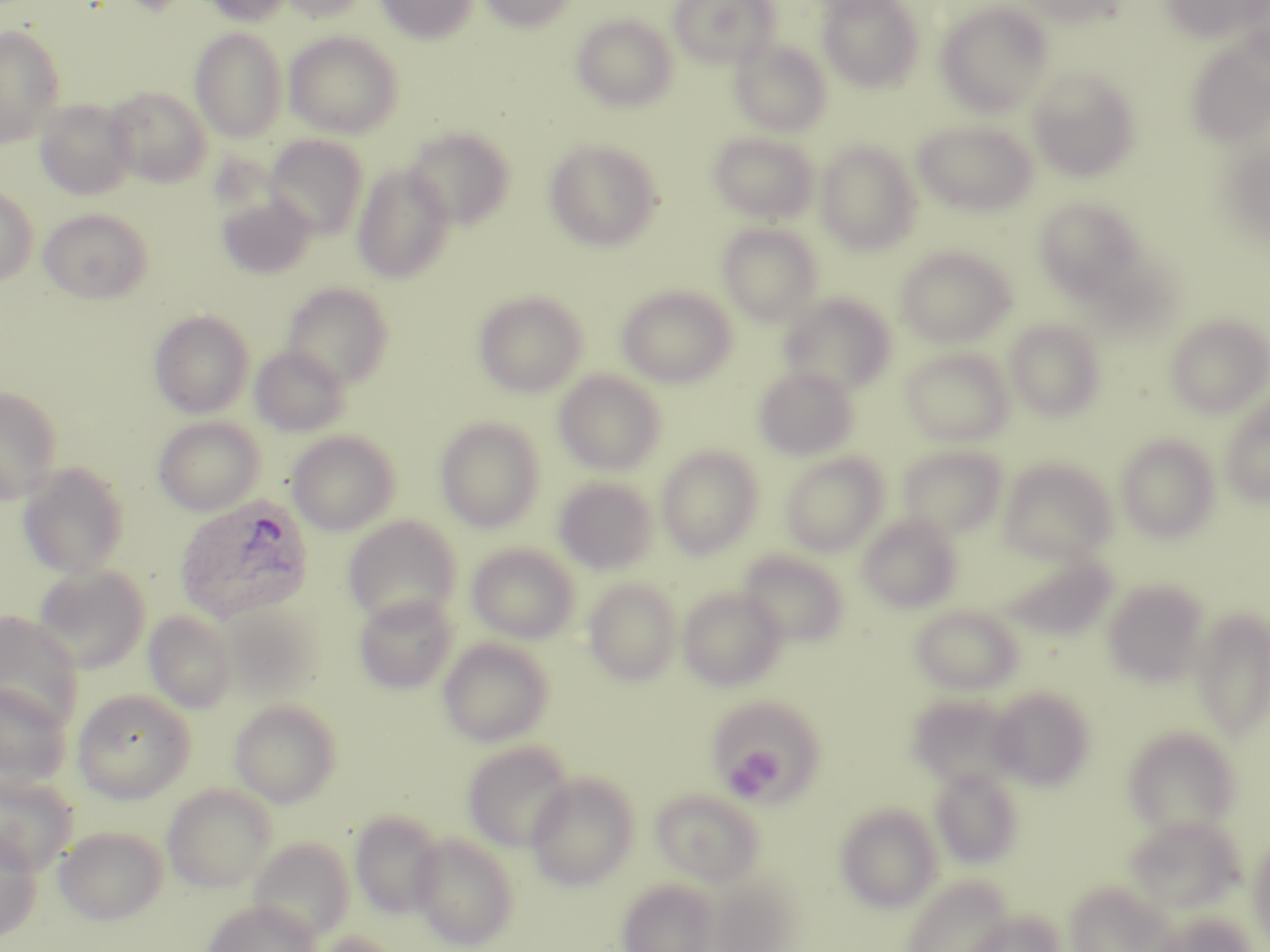
{
  "slide_level_diagnosis": "Plasmodium ovale",
  "field_of_view": "single",
  "preparation": "thin blood film",
  "image_size": "1270×952 pixels",
  "platelet_locations": "approximate bounding boxes as named x1/y1/x2/y2 corners in pixels: (x1=728, y1=745, x2=787, y2=798)",
  "stain": "May-Grünwald-Giemsa",
  "plasmodium_ovale_infected_red_blood_cell_locations": "approximate bounding boxes as named x1/y1/x2/y2 corners in pixels: (x1=174, y1=495, x2=314, y2=623)",
  "magnification": "1000x",
  "modality": "light microscopy",
  "uninfected_red_blood_cell_locations": "approximate bounding boxes as named x1/y1/x2/y2 corners in pixels: (x1=200, y1=0, x2=292, y2=26), (x1=280, y1=0, x2=370, y2=23), (x1=375, y1=0, x2=478, y2=44), (x1=480, y1=0, x2=577, y2=32), (x1=668, y1=0, x2=779, y2=68), (x1=818, y1=0, x2=926, y2=92), (x1=1020, y1=0, x2=1124, y2=27), (x1=1161, y1=0, x2=1269, y2=44), (x1=936, y1=1, x2=1055, y2=115), (x1=571, y1=14, x2=678, y2=112), (x1=0, y1=24, x2=65, y2=148), (x1=190, y1=27, x2=288, y2=143), (x1=284, y1=31, x2=404, y2=139), (x1=1185, y1=35, x2=1270, y2=150), (x1=730, y1=39, x2=831, y2=136), (x1=1027, y1=66, x2=1142, y2=182), (x1=104, y1=86, x2=212, y2=187), (x1=34, y1=98, x2=138, y2=201), (x1=913, y1=120, x2=1038, y2=216), (x1=403, y1=126, x2=515, y2=229), (x1=708, y1=132, x2=818, y2=223), (x1=265, y1=135, x2=368, y2=240), (x1=543, y1=138, x2=663, y2=251), (x1=1227, y1=139, x2=1270, y2=248), (x1=816, y1=141, x2=921, y2=254), (x1=352, y1=165, x2=456, y2=283), (x1=0, y1=186, x2=38, y2=286), (x1=216, y1=193, x2=317, y2=280), (x1=1034, y1=197, x2=1149, y2=304), (x1=38, y1=208, x2=153, y2=304), (x1=717, y1=222, x2=824, y2=325), (x1=894, y1=246, x2=1015, y2=348), (x1=281, y1=282, x2=395, y2=389), (x1=617, y1=285, x2=736, y2=388), (x1=473, y1=290, x2=588, y2=398), (x1=778, y1=292, x2=896, y2=395), (x1=149, y1=310, x2=254, y2=418), (x1=1165, y1=314, x2=1270, y2=418), (x1=1005, y1=318, x2=1106, y2=421), (x1=250, y1=345, x2=351, y2=437), (x1=900, y1=347, x2=1014, y2=446), (x1=753, y1=365, x2=860, y2=461), (x1=554, y1=370, x2=666, y2=475), (x1=0, y1=386, x2=62, y2=501), (x1=1220, y1=396, x2=1270, y2=508), (x1=152, y1=416, x2=265, y2=516), (x1=435, y1=416, x2=545, y2=532), (x1=287, y1=430, x2=401, y2=536), (x1=1116, y1=434, x2=1220, y2=542), (x1=656, y1=445, x2=763, y2=559), (x1=896, y1=445, x2=1008, y2=539), (x1=780, y1=451, x2=889, y2=556), (x1=1000, y1=458, x2=1117, y2=564), (x1=18, y1=462, x2=131, y2=578), (x1=553, y1=477, x2=658, y2=575), (x1=856, y1=513, x2=963, y2=613), (x1=343, y1=516, x2=462, y2=628), (x1=467, y1=542, x2=580, y2=643), (x1=737, y1=550, x2=851, y2=647), (x1=998, y1=550, x2=1117, y2=641), (x1=32, y1=564, x2=151, y2=674), (x1=584, y1=578, x2=682, y2=685), (x1=1102, y1=579, x2=1210, y2=688), (x1=679, y1=587, x2=787, y2=691), (x1=354, y1=594, x2=458, y2=695), (x1=218, y1=604, x2=323, y2=704), (x1=910, y1=605, x2=1024, y2=695), (x1=1190, y1=607, x2=1270, y2=743), (x1=0, y1=611, x2=84, y2=728), (x1=144, y1=611, x2=237, y2=713), (x1=438, y1=637, x2=554, y2=747), (x1=0, y1=682, x2=73, y2=791), (x1=988, y1=686, x2=1096, y2=790), (x1=72, y1=688, x2=196, y2=803), (x1=907, y1=694, x2=1021, y2=790), (x1=229, y1=699, x2=342, y2=807), (x1=712, y1=700, x2=833, y2=811), (x1=1122, y1=726, x2=1242, y2=837), (x1=462, y1=741, x2=575, y2=852), (x1=930, y1=767, x2=1024, y2=868), (x1=0, y1=772, x2=79, y2=874), (x1=526, y1=773, x2=640, y2=890), (x1=162, y1=784, x2=277, y2=892), (x1=650, y1=788, x2=765, y2=887), (x1=834, y1=804, x2=943, y2=912), (x1=349, y1=810, x2=445, y2=918), (x1=1123, y1=815, x2=1245, y2=914), (x1=54, y1=826, x2=168, y2=925), (x1=0, y1=828, x2=42, y2=944), (x1=410, y1=832, x2=520, y2=950), (x1=1247, y1=833, x2=1270, y2=945), (x1=250, y1=838, x2=354, y2=943), (x1=898, y1=875, x2=1015, y2=952), (x1=617, y1=878, x2=720, y2=952), (x1=1065, y1=880, x2=1173, y2=952), (x1=203, y1=900, x2=320, y2=952), (x1=965, y1=910, x2=1065, y2=952), (x1=1152, y1=912, x2=1255, y2=952), (x1=309, y1=931, x2=400, y2=952)"
}